Outline each blood parasite and name the species.
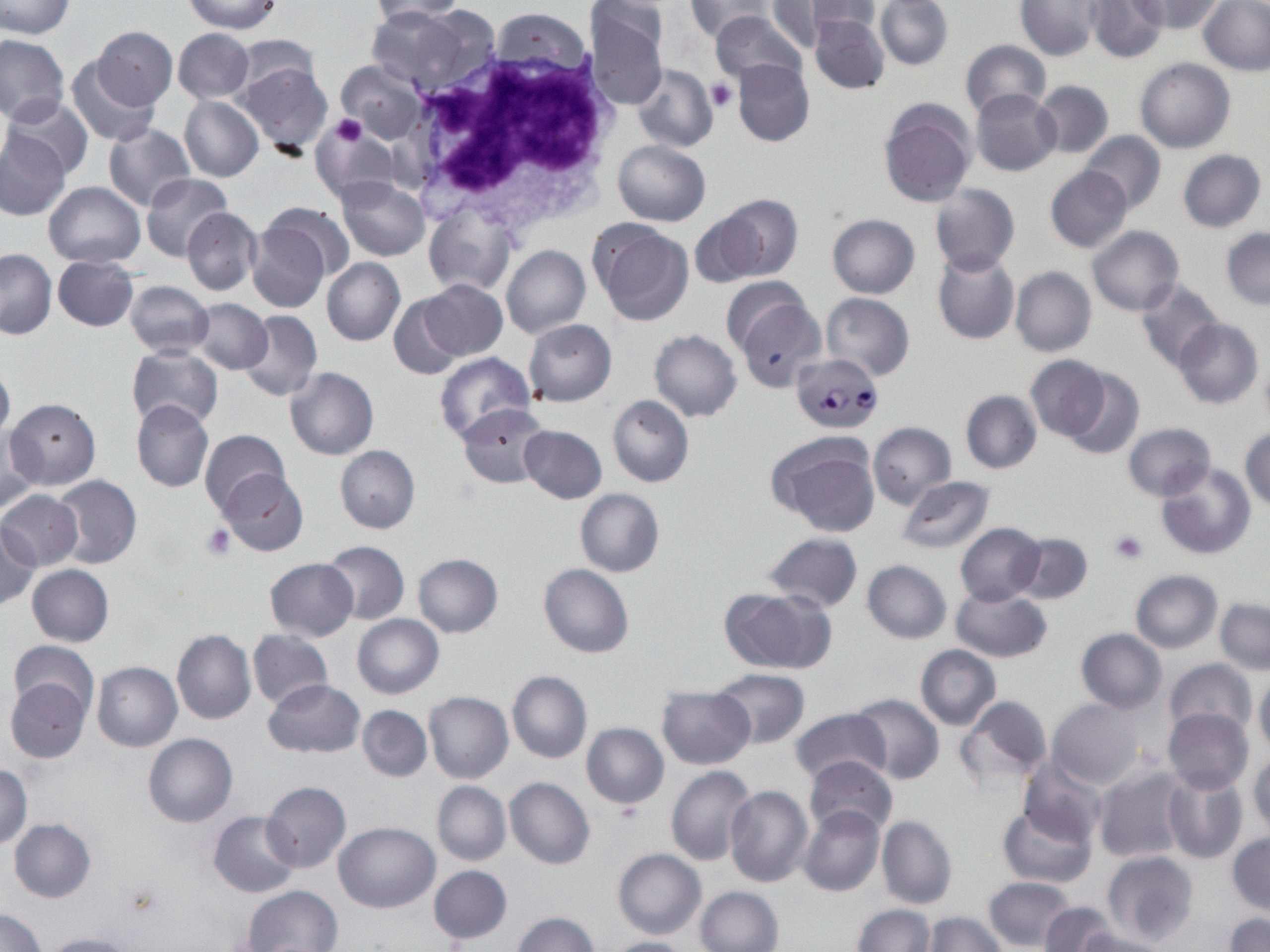
Approximate bounding boxes as (x1, y1, x2, y2) in pixels.
Plasmodium falciparum-infected red blood cells: (789, 353, 884, 432).
No Plasmodium ovale, Plasmodium malariae, Plasmodium vivax, Babesia divergens, or Trypanosoma brucei observed.

Platelet locations: (707, 78, 736, 111), (327, 114, 368, 147), (201, 522, 236, 560), (1108, 530, 1147, 565). Uninfected red blood cell locations: (0, 0, 74, 39), (184, 0, 283, 35), (369, 0, 472, 21), (686, 0, 772, 42), (767, 0, 846, 49), (790, 0, 882, 39), (874, 0, 953, 70), (1016, 0, 1099, 60), (1085, 0, 1167, 62), (1132, 0, 1224, 34), (1176, 0, 1260, 120), (1199, 0, 1270, 75), (3, 2, 71, 86), (367, 5, 469, 95), (585, 5, 668, 110), (711, 10, 806, 87), (810, 11, 890, 94), (93, 26, 176, 108), (172, 29, 253, 104), (0, 35, 69, 125), (958, 39, 1050, 119), (66, 56, 160, 146), (1134, 57, 1234, 153), (234, 58, 334, 157), (336, 58, 426, 144), (732, 59, 814, 147), (632, 64, 717, 152), (1031, 80, 1113, 158), (970, 88, 1062, 176), (3, 96, 94, 181), (180, 96, 263, 183), (878, 100, 975, 208), (310, 121, 400, 209), (102, 125, 194, 210), (0, 129, 69, 220), (1079, 131, 1165, 215), (613, 141, 710, 226), (1177, 148, 1267, 232), (1046, 166, 1132, 253), (140, 173, 233, 262), (336, 177, 429, 260), (43, 182, 145, 267), (928, 183, 1019, 275), (714, 194, 803, 281), (263, 201, 355, 284), (182, 207, 262, 296), (424, 207, 515, 296), (687, 212, 764, 289), (827, 213, 920, 297), (245, 214, 336, 313), (590, 220, 693, 325), (1088, 225, 1184, 315), (1221, 227, 1270, 310), (501, 245, 590, 339), (931, 248, 1019, 345), (0, 249, 55, 339), (53, 254, 139, 330), (321, 258, 405, 345), (1010, 267, 1096, 356), (721, 277, 814, 355), (1133, 278, 1222, 371), (422, 279, 507, 361), (124, 281, 214, 357), (736, 293, 827, 391), (821, 293, 915, 380), (388, 294, 468, 380), (190, 299, 272, 374), (238, 309, 322, 402), (1173, 317, 1262, 409), (524, 318, 616, 406), (648, 331, 741, 422), (126, 346, 223, 430), (434, 352, 534, 445), (1024, 355, 1113, 443), (0, 362, 15, 443), (285, 366, 379, 460), (1060, 366, 1144, 459), (960, 391, 1041, 474), (607, 394, 694, 487), (5, 397, 101, 489), (132, 399, 214, 493), (456, 403, 550, 487), (867, 422, 954, 508), (1123, 423, 1216, 501), (518, 425, 607, 503), (1, 427, 42, 515), (1241, 428, 1270, 513), (199, 429, 290, 517), (767, 432, 880, 535), (336, 445, 420, 533), (1155, 462, 1255, 560), (219, 468, 308, 557), (51, 475, 142, 568), (897, 476, 996, 554), (0, 489, 83, 570), (574, 489, 665, 577), (0, 523, 39, 611), (954, 523, 1045, 606), (761, 532, 863, 611), (1012, 532, 1091, 602), (322, 541, 409, 624), (412, 554, 503, 638), (265, 558, 358, 640), (862, 560, 952, 643), (27, 564, 113, 646), (537, 564, 634, 658), (1130, 570, 1222, 652), (719, 587, 835, 673), (951, 587, 1052, 662), (1215, 598, 1269, 673), (352, 613, 443, 698), (248, 628, 333, 710), (172, 629, 256, 725), (1076, 629, 1166, 712), (10, 642, 99, 721), (915, 645, 1000, 729), (1165, 658, 1256, 738), (92, 661, 182, 751), (709, 668, 810, 747), (507, 671, 591, 764), (1254, 675, 1270, 757), (5, 677, 92, 765), (263, 679, 365, 757), (657, 685, 755, 768), (423, 691, 513, 783), (847, 693, 945, 784), (954, 695, 1052, 791), (1048, 698, 1147, 789), (357, 705, 432, 782), (790, 707, 890, 786), (1163, 707, 1253, 794), (581, 722, 669, 810), (143, 733, 237, 827), (1248, 750, 1269, 834), (805, 756, 898, 838), (1018, 757, 1108, 846), (0, 763, 33, 848), (666, 766, 757, 866), (1092, 766, 1190, 864), (1161, 769, 1247, 864), (504, 776, 594, 869), (260, 781, 351, 873), (432, 781, 510, 865), (725, 785, 813, 887), (798, 804, 885, 898), (996, 804, 1097, 887), (208, 811, 302, 898), (876, 813, 957, 909), (8, 819, 96, 901), (334, 821, 440, 913), (1228, 833, 1270, 915), (613, 848, 707, 939), (1102, 852, 1198, 948), (429, 865, 512, 944), (984, 877, 1078, 951), (243, 884, 342, 951), (695, 886, 782, 952), (1041, 901, 1117, 952), (851, 904, 935, 952), (1, 908, 46, 951), (510, 911, 599, 951), (922, 912, 1006, 952), (1224, 913, 1270, 952), (1071, 929, 1171, 952), (37, 933, 139, 952), (602, 936, 692, 952). White blood cell locations: (400, 37, 619, 233). Slide-level diagnosis: Plasmodium falciparum. 1000x magnification. Image is 1270×952 pixels. One field of a larger specimen. Thin blood smear. May-Grünwald-Giemsa stain. Optical microscopy.